Report the malaria status.
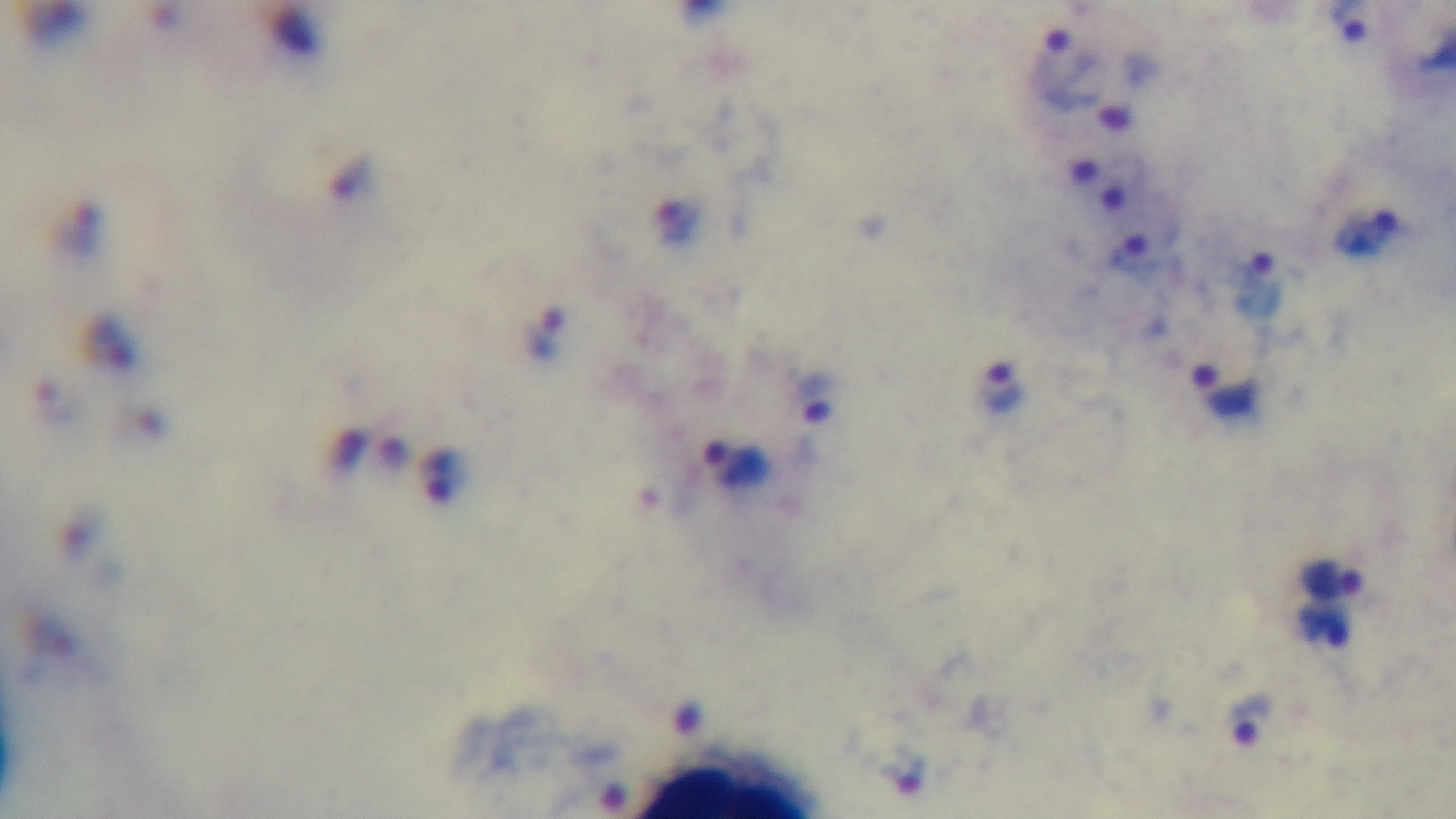

It is infected.

modality: light microscopy
capture: mounted 4K digital camera
objective: 100x oil immersion
stain: Giemsa
field_of_view: single
preparation: thick